Name the parasite shown.
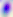

Toxoplasma gondii.

{
  "magnification": "400x",
  "modality": "photomicrograph"
}